Report the malaria status of this cell.
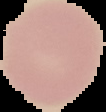

It is uninfected.

Summary:
  - Image size: 106×112 pixels
  - Preparation: thin blood smear
  - Image type: segmented cell region on a black background